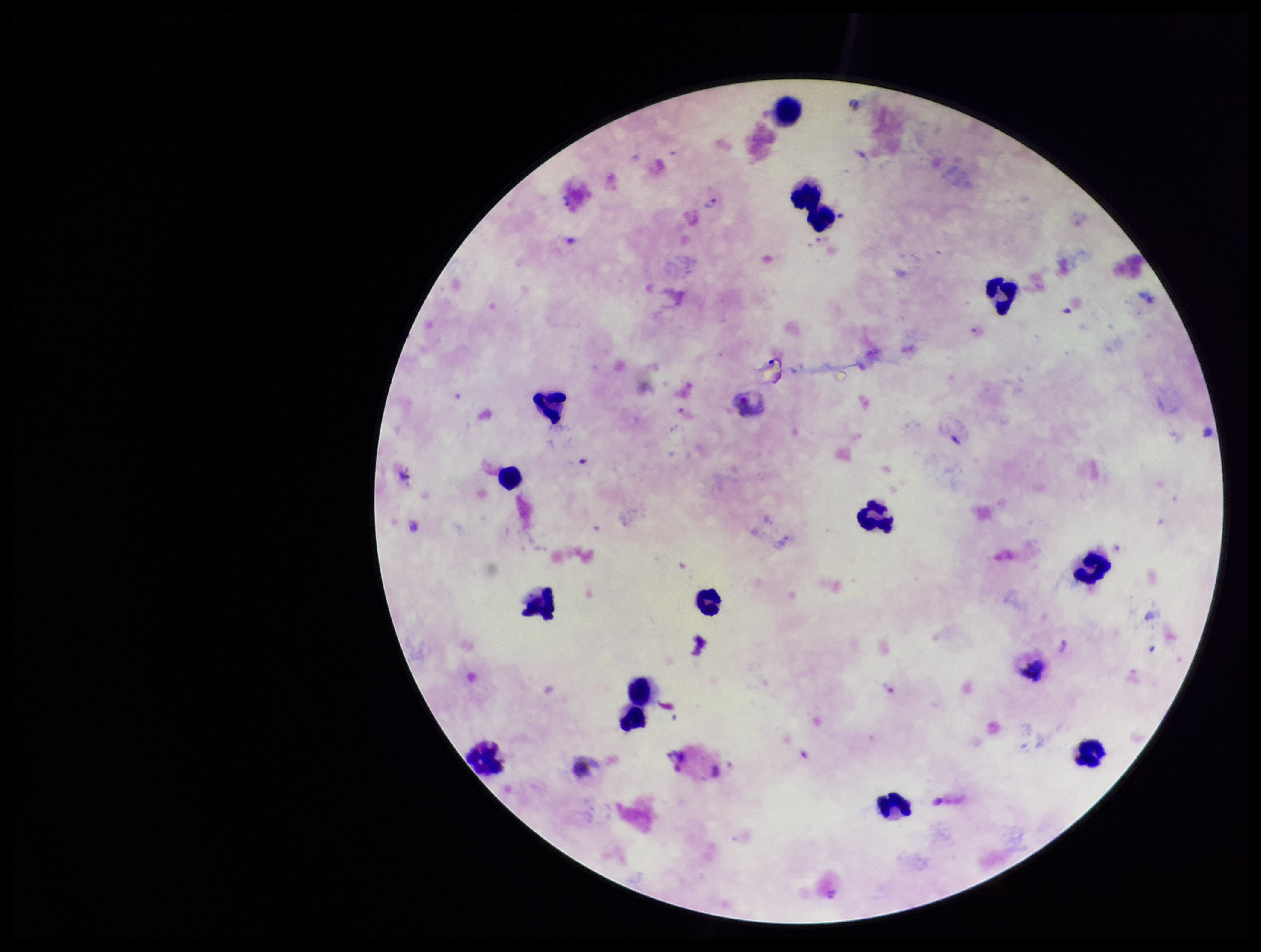
field of view = single
capture = smartphone photograph through the microscope eyepiece
parasite count = 2
species reported for this patient = Plasmodium vivax
Plasmodium parasites = seen
image size = 1261×952 pixels
preparation = thick smear
patient malaria status = infected
leukocyte count = 13
stain = Giemsa